Locate every blood parasite and identify its species.
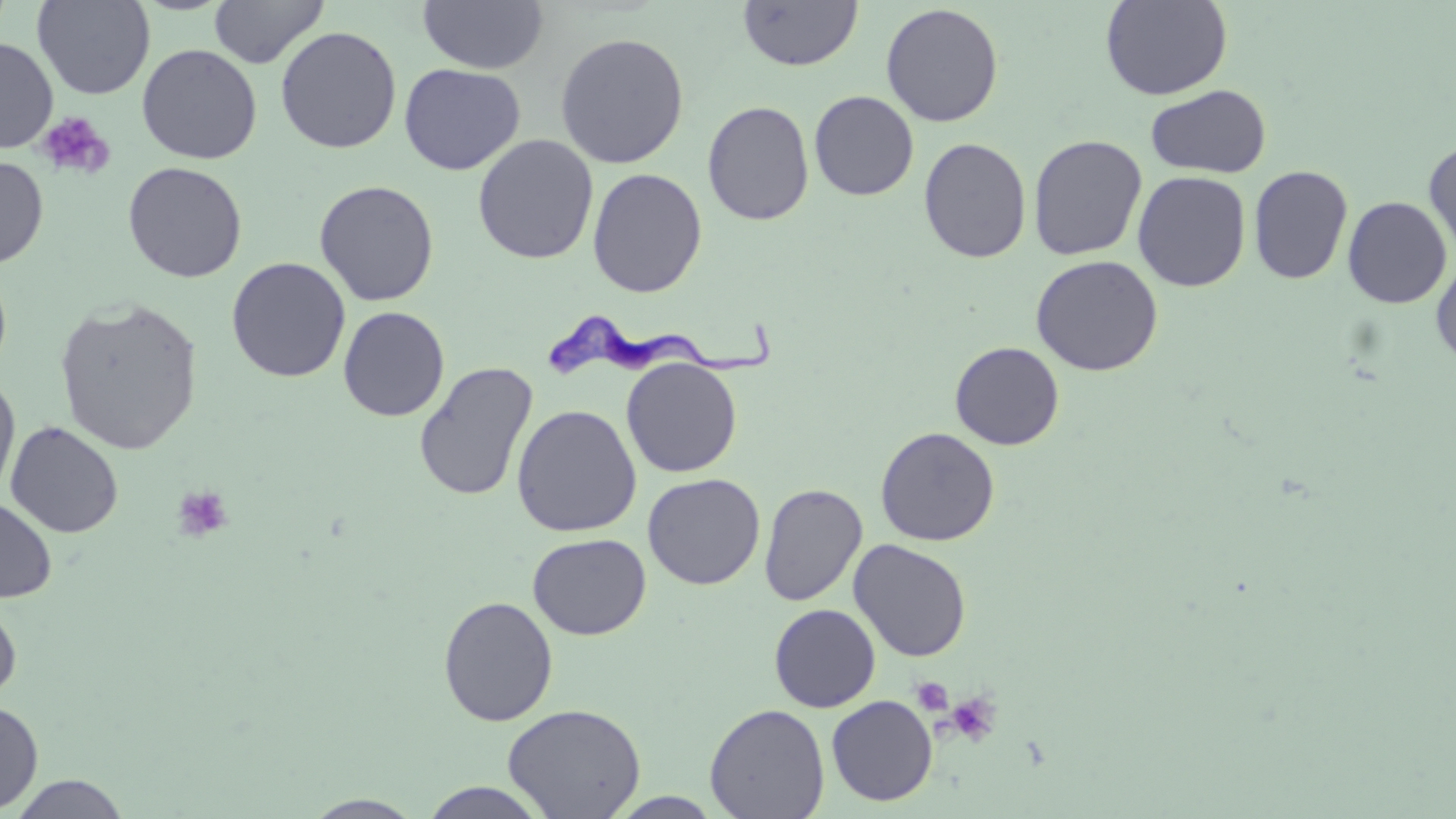

Approximate bounding boxes as (x1, y1, x2, y2) in pixels.
Trypanosoma brucei: (542, 306, 787, 380).
No Plasmodium falciparum, Plasmodium ovale, Plasmodium malariae, Plasmodium vivax, or Babesia divergens observed.

slide-level diagnosis = Trypanosoma brucei
field of view = one of a larger specimen
uninfected red blood cell locations = approximate bounding boxes as (x1, y1, x2, y2) in pixels: (32, 0, 155, 99), (208, 0, 329, 68), (417, 0, 548, 75), (1100, 0, 1233, 100), (738, 1, 863, 71), (880, 3, 1004, 127), (275, 25, 402, 154), (554, 32, 690, 168), (0, 37, 58, 153), (136, 44, 262, 164), (398, 63, 526, 174), (1146, 84, 1271, 178), (809, 90, 919, 201), (702, 100, 815, 225), (472, 134, 599, 265), (1028, 134, 1147, 260), (919, 137, 1032, 264), (1423, 138, 1456, 261), (0, 155, 49, 268), (122, 161, 248, 283), (1248, 165, 1353, 285), (588, 168, 707, 297), (1132, 170, 1251, 291), (314, 179, 439, 306), (1343, 196, 1452, 309), (1030, 254, 1163, 375), (1431, 255, 1456, 367), (226, 257, 350, 382), (0, 263, 13, 383), (53, 297, 203, 456), (338, 306, 449, 422), (949, 342, 1065, 450), (621, 358, 742, 477), (413, 361, 538, 502), (0, 374, 21, 503), (511, 403, 642, 537), (5, 420, 124, 538), (875, 426, 1000, 546), (643, 473, 765, 590), (759, 483, 867, 606), (0, 497, 57, 603), (527, 533, 652, 640), (848, 539, 972, 662), (438, 596, 558, 727), (0, 597, 21, 705), (768, 603, 881, 712), (826, 695, 937, 806), (0, 700, 43, 814), (502, 703, 647, 818), (704, 703, 830, 819), (7, 774, 131, 818), (418, 781, 551, 818), (300, 794, 426, 818)
magnification = 1000x
platelet locations = approximate bounding boxes as (x1, y1, x2, y2) in pixels: (37, 111, 115, 180), (172, 486, 234, 542), (911, 677, 953, 716), (945, 692, 1001, 747)
modality = light microscopy
image size = 1456×819 pixels
preparation = thin blood smear
stain = May-Grünwald-Giemsa